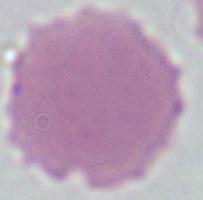

Summary:
  - Magnification: 1000x
  - Modality: photomicrograph
  - Identification: red blood cell